Point out each malaria parasite and each leukocyte.
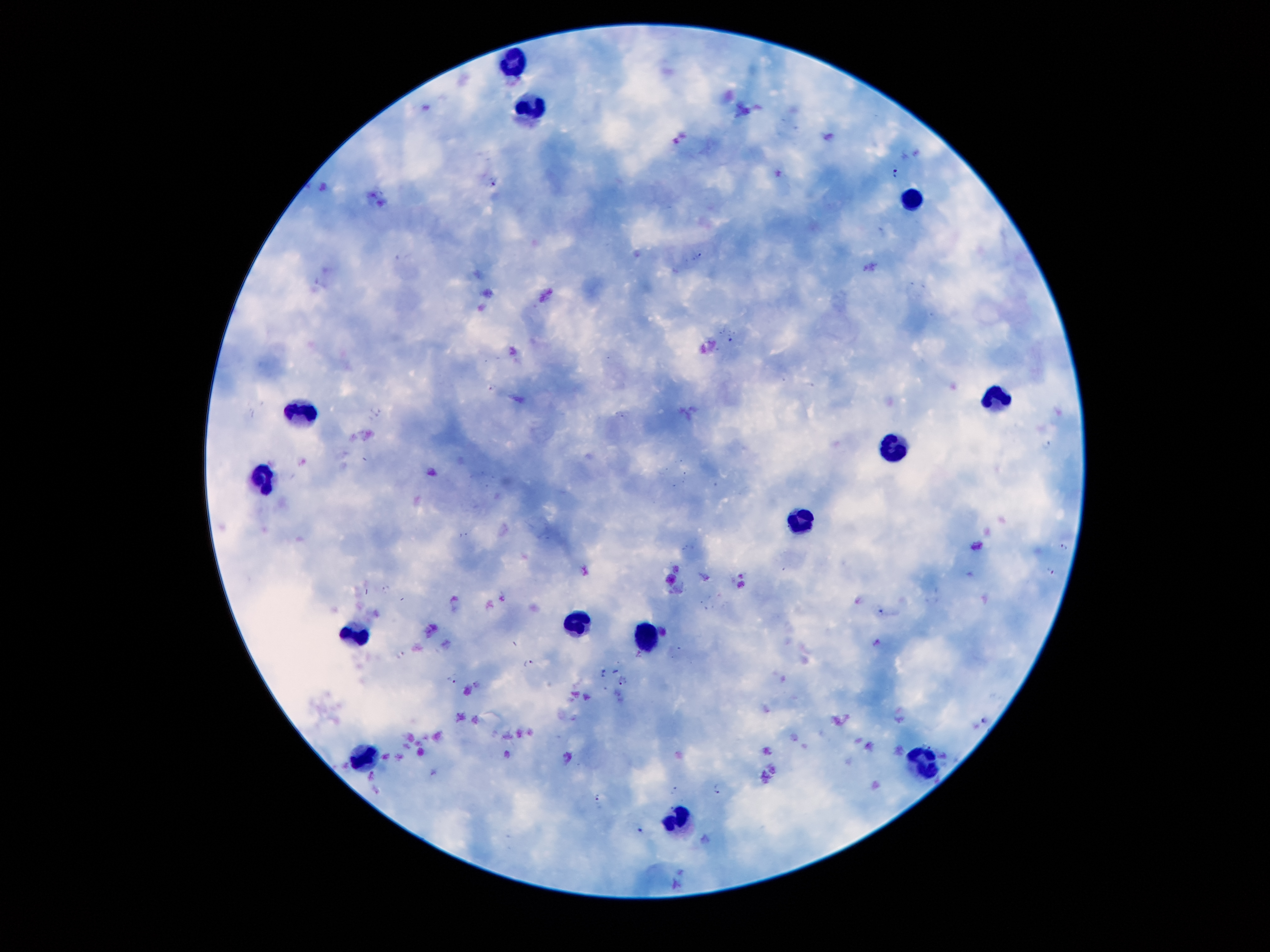
Approximate centers as [x, y] in pixels.
Malaria parasites: [894, 171], [493, 180], [700, 255], [729, 339], [492, 386], [1046, 444], [1063, 547], [1049, 572], [385, 588], [880, 611], [400, 654], [528, 663], [450, 679], [623, 680], [983, 719], [716, 788], [675, 789], [598, 797], [639, 828].
Leukocytes: [509, 67], [529, 110], [913, 203], [994, 401], [303, 414], [894, 448], [261, 475], [807, 519], [571, 624], [354, 635], [650, 638], [361, 754], [924, 764], [676, 813].

Patient malaria status: infected with Plasmodium falciparum. 100x magnification. Single field of view. Image is 1270×952 pixels. Thick blood smear. Giemsa-stained preparation. Photographed through the microscope eyepiece with a smartphone camera.